Locate every blood parasite and identify its species.
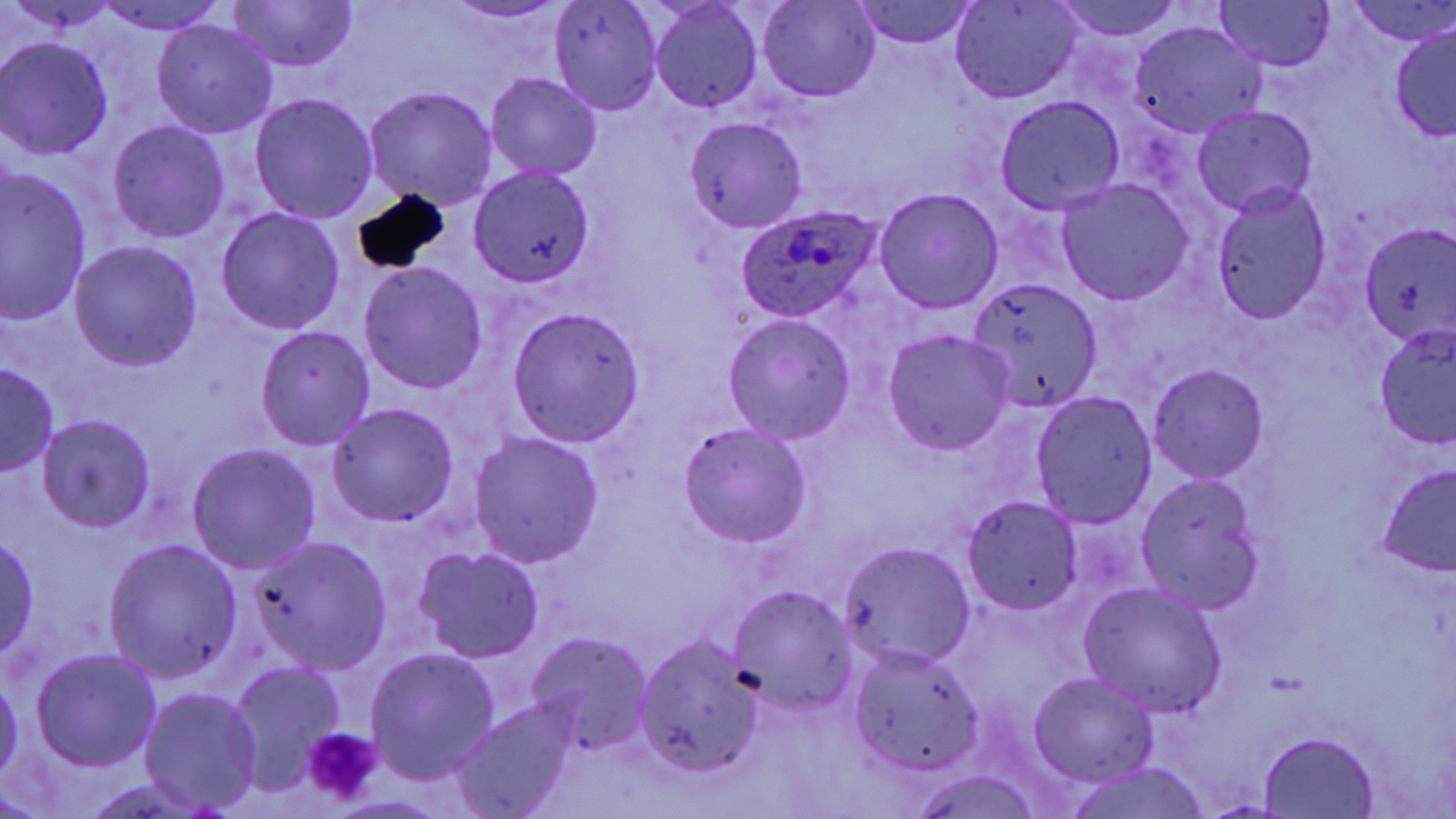

Approximate bounding boxes as (x1,y1)-(x2,y2) corner pairs in pixels.
Plasmodium ovale-infected red blood cells: (736,204)-(885,322).
No Plasmodium falciparum, Plasmodium malariae, Plasmodium vivax, Babesia divergens, or Trypanosoma brucei observed.

Uninfected red blood cell locations: (11,0)-(119,35), (438,0)-(575,24), (757,0)-(879,101), (1049,0)-(1188,42), (1216,0)-(1335,71), (1349,0)-(1456,47), (226,1)-(357,72), (951,1)-(1082,103), (97,2)-(226,36), (550,2)-(663,116), (851,2)-(978,49), (650,3)-(763,113), (152,19)-(278,139), (1128,20)-(1268,140), (1390,23)-(1456,142), (0,37)-(116,159), (486,72)-(601,179), (363,86)-(498,208), (249,92)-(379,222), (995,95)-(1125,214), (1194,105)-(1317,216), (684,116)-(808,233), (108,120)-(230,243), (470,168)-(595,286), (1,169)-(93,324), (1056,179)-(1194,304), (1211,184)-(1331,322), (874,188)-(1004,314), (216,205)-(346,334), (1361,227)-(1456,341), (70,241)-(202,370), (359,262)-(489,395), (966,277)-(1102,411), (507,307)-(644,445), (723,315)-(858,443), (1374,325)-(1455,449), (256,326)-(376,449), (883,330)-(1014,455), (0,361)-(58,476), (1148,363)-(1269,481), (1031,392)-(1157,527), (326,403)-(459,526), (38,415)-(156,532), (679,423)-(813,546), (468,431)-(604,567), (189,444)-(320,575), (1375,462)-(1456,581), (1139,476)-(1266,610), (962,497)-(1084,615), (0,535)-(40,659), (251,537)-(391,674), (104,539)-(241,682), (837,543)-(975,670), (414,546)-(544,663), (1078,581)-(1228,717), (729,586)-(856,714), (527,632)-(653,757), (635,636)-(762,776), (850,647)-(983,777), (365,648)-(500,782), (33,650)-(163,770), (227,662)-(344,792), (1029,671)-(1158,787), (0,678)-(22,786), (142,688)-(263,813), (454,701)-(574,818), (1259,731)-(1378,817), (1064,763)-(1213,819), (903,769)-(1048,819). Platelet locations: (301,727)-(381,805). Slide-level diagnosis: Plasmodium ovale. Image is 1456×819 pixels. 1000x magnification. Single field of view. Optical microscopy. Thin blood film. May-Grünwald-Giemsa-stained preparation.